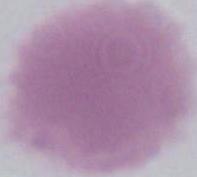
Summary:
  - Identification: red blood cell
  - Modality: micrograph
  - Magnification: 1000x